Name the blood parasite species.
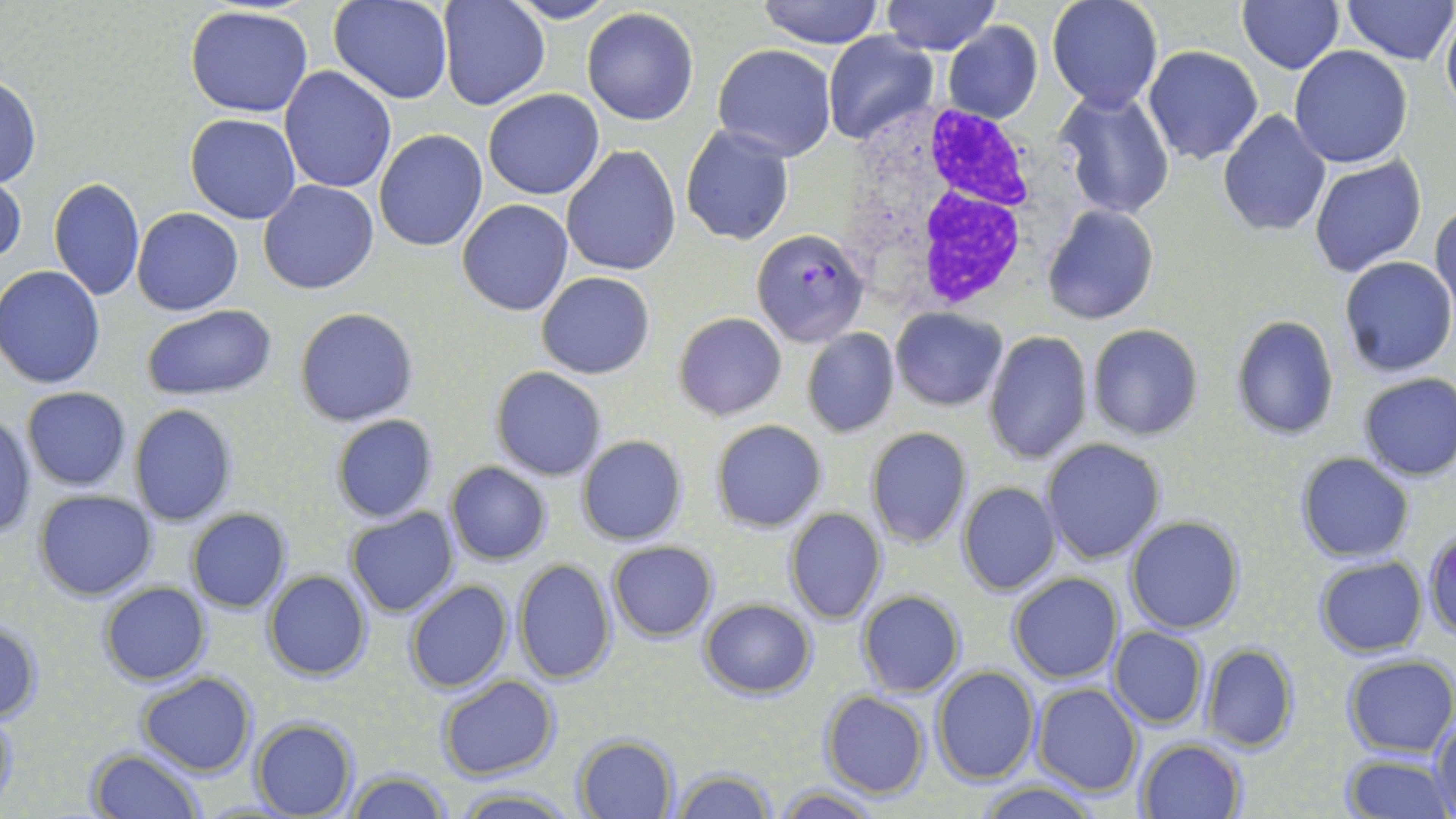
Plasmodium falciparum.

stain = May-Grünwald-Giemsa
preparation = thin blood film
uninfected red blood cell locations = approximate bounding boxes as named x1/y1/x2/y2 corners in pixels: (x1=756, y1=0, x2=885, y2=48), (x1=881, y1=0, x2=999, y2=55), (x1=1046, y1=0, x2=1163, y2=112), (x1=1343, y1=0, x2=1455, y2=65), (x1=328, y1=1, x2=453, y2=105), (x1=437, y1=1, x2=549, y2=111), (x1=507, y1=1, x2=619, y2=24), (x1=1238, y1=1, x2=1344, y2=73), (x1=894, y1=5, x2=1032, y2=84), (x1=1440, y1=5, x2=1456, y2=121), (x1=185, y1=6, x2=314, y2=116), (x1=581, y1=8, x2=700, y2=126), (x1=943, y1=23, x2=1043, y2=124), (x1=822, y1=32, x2=937, y2=145), (x1=713, y1=45, x2=837, y2=162), (x1=1143, y1=45, x2=1264, y2=165), (x1=1289, y1=45, x2=1414, y2=168), (x1=280, y1=66, x2=396, y2=194), (x1=0, y1=76, x2=41, y2=188), (x1=1054, y1=87, x2=1175, y2=219), (x1=483, y1=89, x2=604, y2=199), (x1=1218, y1=110, x2=1333, y2=237), (x1=186, y1=113, x2=302, y2=224), (x1=681, y1=125, x2=794, y2=245), (x1=374, y1=129, x2=488, y2=251), (x1=561, y1=145, x2=681, y2=276), (x1=1310, y1=157, x2=1428, y2=279), (x1=0, y1=174, x2=26, y2=270), (x1=48, y1=177, x2=145, y2=300), (x1=259, y1=180, x2=379, y2=294), (x1=458, y1=200, x2=573, y2=316), (x1=1431, y1=200, x2=1456, y2=319), (x1=1042, y1=204, x2=1158, y2=325), (x1=132, y1=207, x2=243, y2=315), (x1=1337, y1=256, x2=1455, y2=376), (x1=0, y1=266, x2=106, y2=388), (x1=537, y1=271, x2=655, y2=378), (x1=143, y1=305, x2=277, y2=399), (x1=294, y1=308, x2=417, y2=426), (x1=891, y1=308, x2=1007, y2=411), (x1=674, y1=312, x2=786, y2=422), (x1=1230, y1=315, x2=1339, y2=440), (x1=1086, y1=324, x2=1204, y2=441), (x1=801, y1=328, x2=899, y2=437), (x1=984, y1=331, x2=1093, y2=465), (x1=489, y1=366, x2=607, y2=481), (x1=1357, y1=372, x2=1456, y2=481), (x1=21, y1=386, x2=133, y2=491), (x1=128, y1=403, x2=238, y2=527), (x1=1, y1=413, x2=37, y2=537), (x1=331, y1=415, x2=439, y2=523), (x1=711, y1=419, x2=827, y2=533), (x1=866, y1=427, x2=971, y2=548), (x1=576, y1=434, x2=688, y2=545), (x1=1041, y1=439, x2=1166, y2=564), (x1=1296, y1=452, x2=1415, y2=562), (x1=444, y1=462, x2=552, y2=565), (x1=957, y1=482, x2=1061, y2=596), (x1=33, y1=490, x2=158, y2=601), (x1=783, y1=507, x2=887, y2=624), (x1=345, y1=508, x2=460, y2=618), (x1=186, y1=509, x2=292, y2=612), (x1=1124, y1=515, x2=1244, y2=635), (x1=1425, y1=528, x2=1456, y2=639), (x1=607, y1=541, x2=718, y2=641), (x1=1314, y1=556, x2=1426, y2=657), (x1=513, y1=559, x2=616, y2=684), (x1=262, y1=570, x2=371, y2=680), (x1=1007, y1=573, x2=1124, y2=683), (x1=99, y1=581, x2=210, y2=686), (x1=404, y1=581, x2=514, y2=694), (x1=856, y1=590, x2=966, y2=697), (x1=698, y1=598, x2=817, y2=698), (x1=0, y1=622, x2=42, y2=722), (x1=1108, y1=627, x2=1207, y2=728), (x1=1200, y1=643, x2=1297, y2=751), (x1=1341, y1=653, x2=1456, y2=758), (x1=932, y1=665, x2=1041, y2=785), (x1=137, y1=671, x2=256, y2=777), (x1=436, y1=675, x2=559, y2=780), (x1=1032, y1=684, x2=1142, y2=798), (x1=820, y1=691, x2=931, y2=800), (x1=0, y1=708, x2=20, y2=810), (x1=1431, y1=711, x2=1456, y2=817), (x1=249, y1=718, x2=358, y2=818), (x1=575, y1=734, x2=679, y2=819), (x1=1134, y1=737, x2=1247, y2=819), (x1=87, y1=748, x2=204, y2=819), (x1=1340, y1=753, x2=1451, y2=818), (x1=671, y1=765, x2=776, y2=818), (x1=343, y1=771, x2=453, y2=819), (x1=975, y1=780, x2=1099, y2=818), (x1=771, y1=785, x2=885, y2=819), (x1=452, y1=786, x2=578, y2=819)
field of view = single
image size = 1456×819 pixels
white blood cell locations = approximate bounding boxes as named x1/y1/x2/y2 corners in pixels: (x1=843, y1=104, x2=1052, y2=317)
magnification = 1000x
modality = light microscopy
Plasmodium falciparum-infected red blood cell locations = approximate bounding boxes as named x1/y1/x2/y2 corners in pixels: (x1=752, y1=228, x2=870, y2=348)